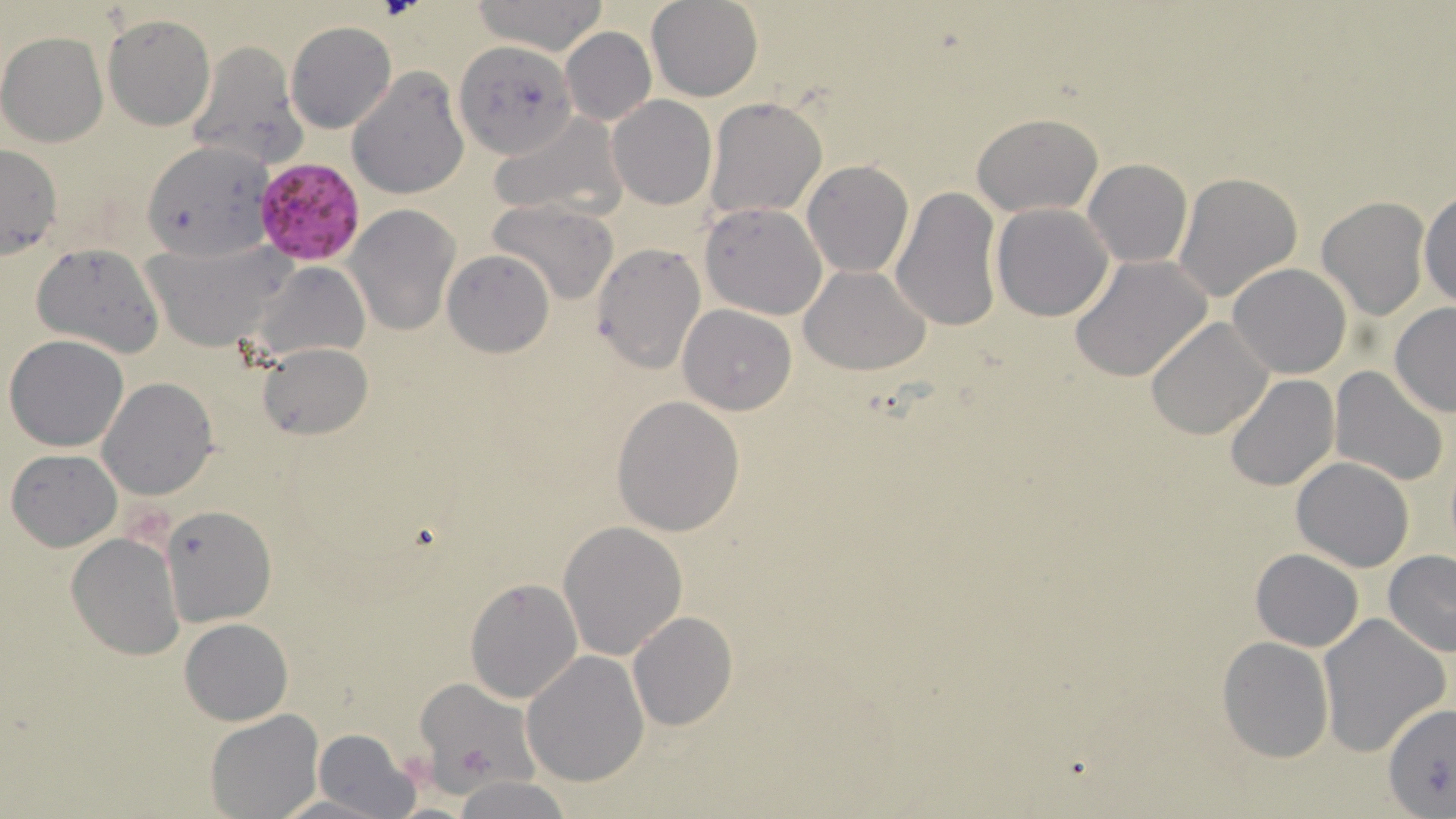
Summary:
  - Coordinate format: approximate bounding boxes as (x1,y1)-(x2,y2) corner pairs in pixels
  - Plasmodium falciparum-infected red blood cell locations: (259,162)-(370,269)
  - Uninfected red blood cell locations: (468,0)-(610,54), (647,0)-(762,101), (104,15)-(215,131), (286,21)-(396,133), (559,27)-(655,126), (1,31)-(110,147), (185,39)-(305,169), (454,40)-(579,159), (347,69)-(469,197), (607,96)-(717,210), (703,97)-(828,220), (489,112)-(625,221), (973,113)-(1103,217), (143,141)-(274,259), (0,145)-(63,260), (802,160)-(914,278), (1083,160)-(1192,268), (800,171)-(1002,298), (1173,172)-(1303,304), (890,186)-(1003,332), (1418,187)-(1456,311), (1317,198)-(1430,320), (489,199)-(619,305), (699,202)-(827,320), (990,202)-(1114,321), (345,205)-(459,335), (142,240)-(293,350), (31,242)-(165,358), (591,244)-(705,372), (442,250)-(553,358), (1069,255)-(1213,381), (253,257)-(372,360), (1228,263)-(1352,378), (799,265)-(932,377), (1388,302)-(1456,417), (679,305)-(797,415), (1145,317)-(1274,440), (5,335)-(130,452), (258,342)-(372,441), (1329,366)-(1450,485), (1224,375)-(1338,492), (98,378)-(217,499), (611,397)-(744,537), (6,448)-(122,551), (1291,457)-(1415,572), (160,503)-(276,627), (558,520)-(688,661), (67,532)-(185,660), (1250,548)-(1363,652), (1382,550)-(1456,656), (465,576)-(582,703), (627,613)-(737,730), (1317,613)-(1450,758), (179,618)-(293,725), (1217,637)-(1335,762), (522,650)-(650,787), (415,679)-(536,788), (1384,704)-(1456,818), (206,708)-(322,817), (313,728)-(422,819), (454,776)-(575,818), (268,793)-(396,819)
  - Slide-level diagnosis: Plasmodium falciparum
  - Field of view: one of a larger specimen
  - Image size: 1456×819 pixels
  - Magnification: 1000x
  - Preparation: thin blood smear
  - Stain: May-Grünwald-Giemsa
  - Modality: light microscopy